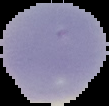

Cell region segmented out of the field of view; the surrounding area is masked to black. Result: no malaria parasites detected. From a thin blood smear. Image is 109×106 pixels.